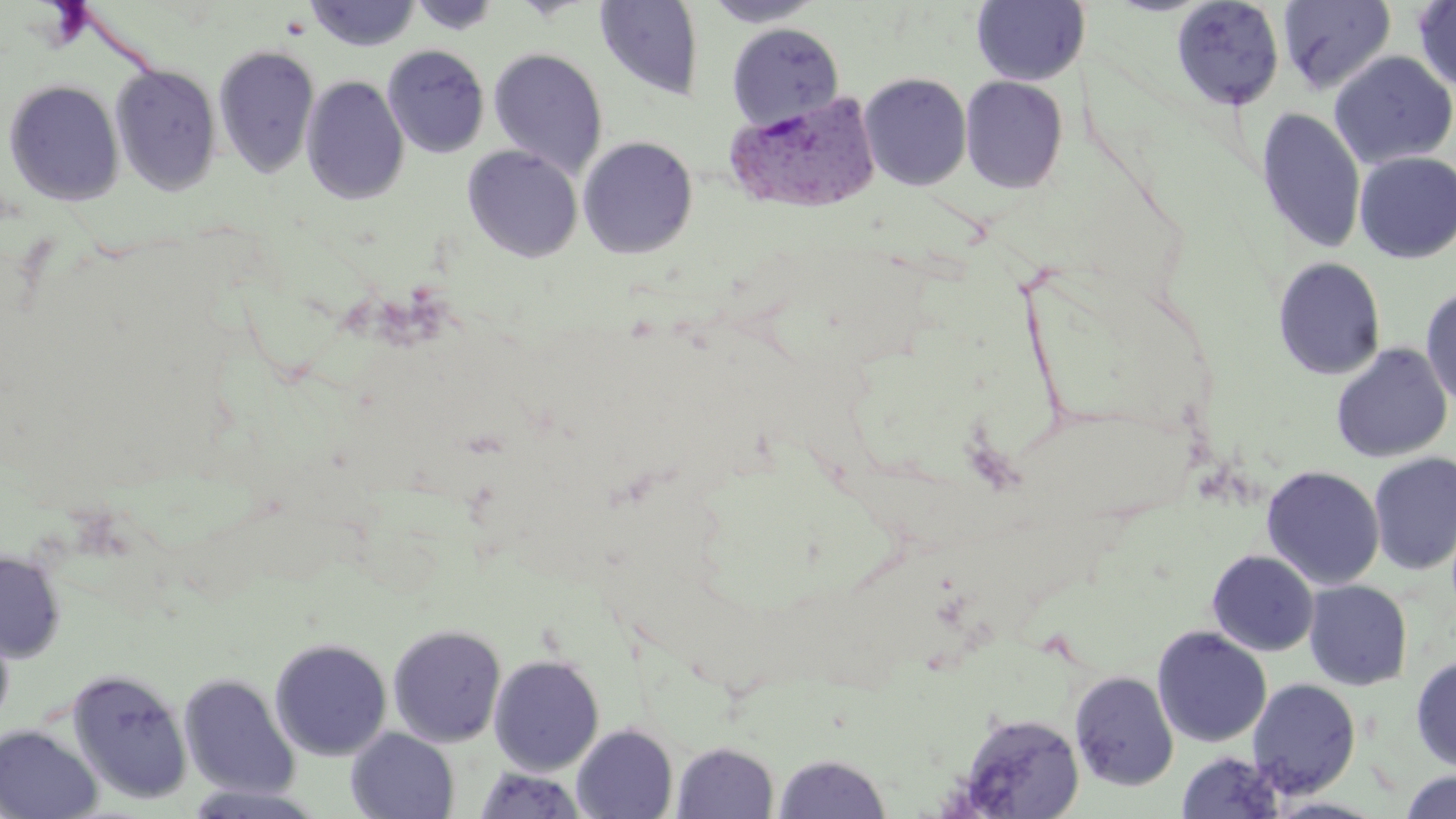
Summary:
  - Coordinate format: approximate bounding boxes as (x1,y1)-(x2,y2) corner pairs in pixels
  - Uninfected red blood cell locations: (408,0)-(502,35), (701,0)-(827,27), (1277,0)-(1396,95), (305,1)-(422,51), (594,1)-(704,101), (971,1)-(1091,86), (1170,1)-(1285,111), (1412,1)-(1456,94), (727,22)-(845,131), (213,44)-(320,180), (382,44)-(490,159), (488,47)-(609,180), (1329,50)-(1456,170), (110,63)-(222,196), (859,72)-(973,191), (301,75)-(409,205), (960,75)-(1068,194), (3,78)-(125,206), (1256,108)-(1366,255), (577,135)-(699,260), (462,145)-(583,263), (1354,152)-(1456,264), (1272,257)-(1387,380), (1420,284)-(1456,413), (1330,343)-(1453,463), (1368,451)-(1456,576), (1261,465)-(1385,590), (0,550)-(66,663), (1206,550)-(1319,656), (1303,580)-(1413,691), (0,618)-(15,733), (387,624)-(507,748), (1152,626)-(1272,748), (269,637)-(392,761), (488,653)-(605,775), (1411,655)-(1456,773), (66,667)-(193,806), (1068,670)-(1179,791), (178,673)-(300,799), (1247,678)-(1362,799), (953,712)-(1085,818), (571,724)-(678,819), (0,725)-(102,819), (346,728)-(459,819), (671,741)-(780,819), (1176,751)-(1285,818), (772,752)-(892,818), (472,765)-(589,819), (1400,770)-(1456,818), (179,783)-(330,818), (1265,796)-(1390,818)
  - Plasmodium vivax-infected red blood cell locations: (723,92)-(881,214)
  - Slide-level diagnosis: Plasmodium vivax
  - Image size: 1456×819 pixels
  - Magnification: 1000x
  - Stain: May-Grünwald-Giemsa
  - Field of view: one of a larger specimen
  - Preparation: thin blood film
  - Modality: optical microscopy